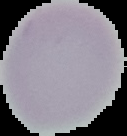
The area outside the segmented cell region is set to black. Result: no Plasmodium parasites seen. From a thin blood film. Image is 127×136 pixels.